Evaluate for malaria.
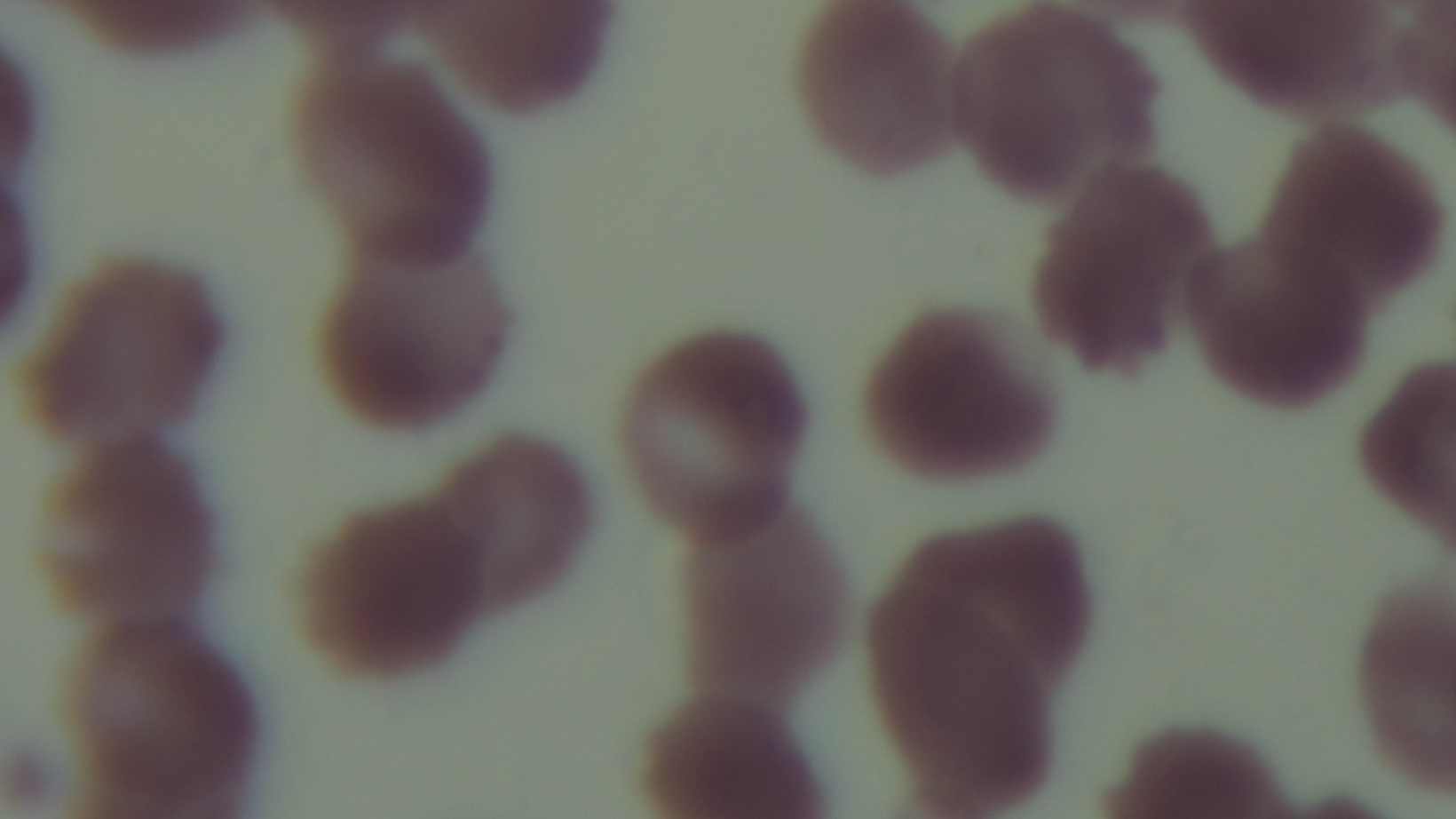
Uninfected.

Giemsa-stained. One field from the slide. Preparation: thin. Mounted 4K digital camera. 100x oil-immersion objective. Photomicrograph.